Locate every blood parasite and identify its species.
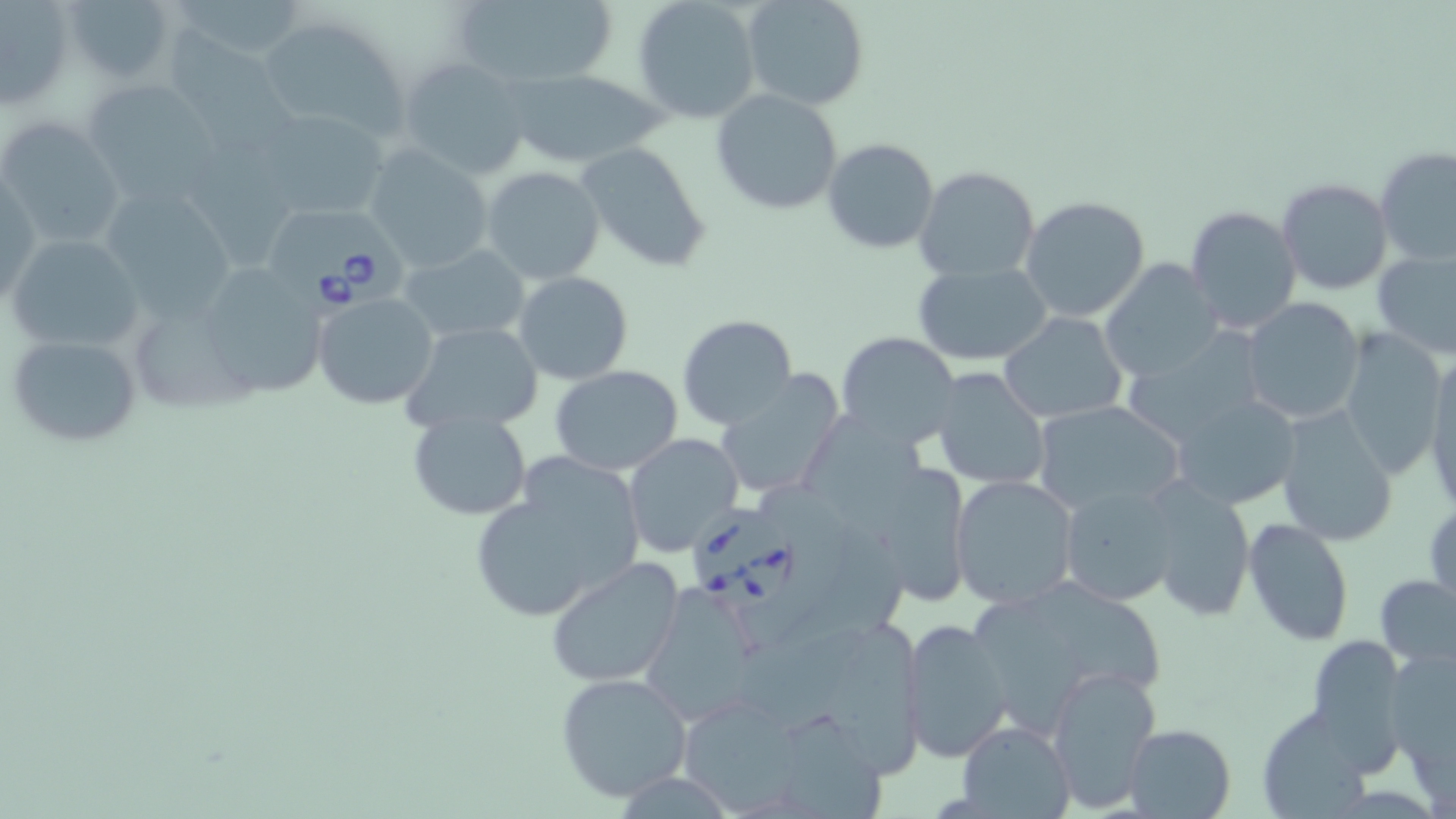

Approximate bounding boxes as (x1,y1)-(x2,y2) corner pairs in pixels.
Babesia divergens-infected red blood cells: (270,200)-(409,320), (689,502)-(796,606).
No Plasmodium falciparum, Plasmodium ovale, Plasmodium malariae, Plasmodium vivax, or Trypanosoma brucei observed.

slide-level diagnosis = Babesia divergens
preparation = thin blood film
field of view = one of a larger specimen
stain = May-Grünwald-Giemsa
magnification = 1000x
modality = light microscopy
image size = 1456×819 pixels
uninfected red blood cell locations = approximate bounding boxes as (x1,y1)-(x2,y2) corner pairs in pixels: (63,0)-(179,86), (170,0)-(312,63), (450,0)-(620,88), (631,0)-(763,122), (741,0)-(870,112), (0,2)-(77,109), (256,14)-(412,145), (165,21)-(297,170), (399,55)-(533,180), (507,69)-(667,168), (80,78)-(223,202), (710,89)-(843,214), (254,107)-(390,221), (0,118)-(124,251), (821,132)-(939,248), (191,136)-(297,267), (575,140)-(711,271), (362,145)-(495,274), (1375,145)-(1456,267), (480,165)-(607,285), (913,166)-(1040,282), (1,172)-(43,303), (1278,178)-(1393,295), (103,184)-(242,326), (1019,196)-(1151,322), (1186,205)-(1302,335), (7,232)-(144,354), (399,243)-(530,346), (1373,248)-(1456,360), (1099,259)-(1222,382), (912,260)-(1053,366), (210,263)-(330,400), (513,271)-(633,385), (313,293)-(439,408), (1240,297)-(1363,425), (999,312)-(1128,423), (677,314)-(798,430), (129,317)-(265,418), (400,322)-(544,433), (1339,327)-(1446,478), (834,331)-(960,447), (6,332)-(144,449), (1119,332)-(1267,452), (1422,351)-(1456,514), (550,366)-(683,476), (931,366)-(1051,489), (714,371)-(846,502), (1170,394)-(1301,510), (1032,399)-(1183,515), (1275,404)-(1400,546), (406,409)-(533,520), (800,414)-(924,535), (624,433)-(741,554), (526,441)-(745,579), (468,455)-(644,624), (858,460)-(974,602), (949,474)-(1079,609), (1142,477)-(1256,622), (1060,483)-(1181,606), (1426,496)-(1456,612), (1242,517)-(1355,647), (544,556)-(686,688), (1376,574)-(1456,669), (1038,578)-(1162,697), (640,584)-(762,723), (973,598)-(1089,736), (829,616)-(930,784), (900,618)-(1013,764), (1305,633)-(1407,765), (1383,645)-(1455,777), (1047,666)-(1160,811), (554,672)-(693,802), (679,698)-(802,819), (1260,706)-(1372,818), (782,712)-(887,819), (956,721)-(1074,819), (1124,723)-(1235,818)